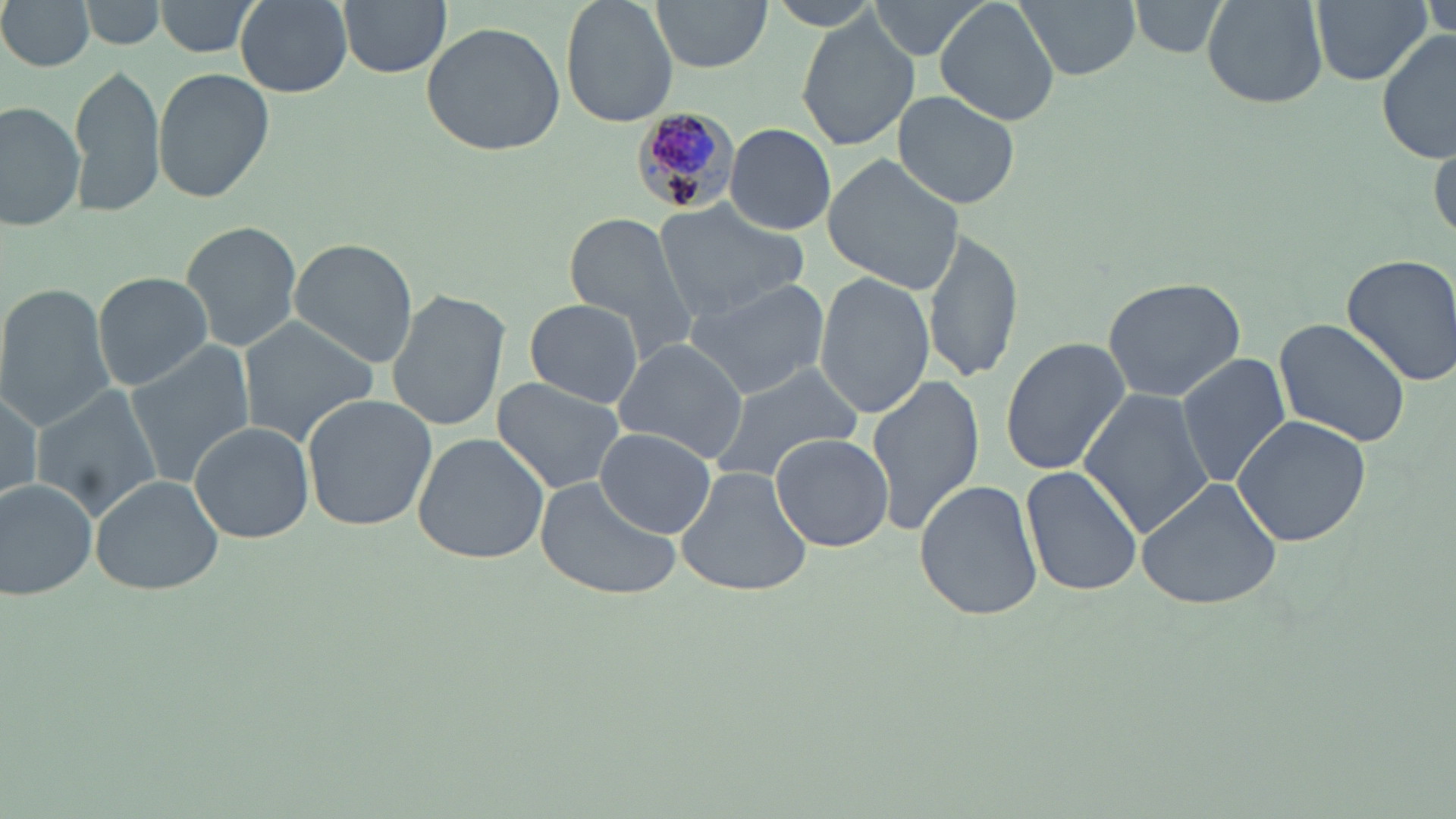

Summary:
  - Coordinate format: approximate bounding boxes as [x1, y1, x2, y2] in pixels
  - Plasmodium malariae-infected red blood cell locations: [630, 106, 742, 220]
  - Uninfected red blood cell locations: [0, 0, 98, 72], [82, 0, 167, 49], [154, 0, 263, 56], [338, 0, 450, 78], [560, 0, 679, 127], [650, 0, 773, 72], [867, 0, 992, 64], [936, 0, 1059, 126], [1015, 0, 1140, 81], [1122, 0, 1239, 58], [1206, 0, 1330, 106], [1310, 0, 1429, 85], [1423, 0, 1454, 42], [235, 1, 353, 97], [797, 14, 918, 153], [421, 21, 565, 158], [1376, 31, 1454, 165], [70, 64, 168, 221], [152, 66, 274, 203], [892, 90, 1022, 210], [1, 101, 85, 232], [725, 123, 836, 236], [1429, 131, 1455, 245], [822, 154, 965, 295], [654, 199, 810, 320], [562, 211, 702, 370], [180, 219, 303, 355], [922, 228, 1023, 387], [287, 238, 419, 367], [1340, 251, 1456, 389], [815, 271, 934, 420], [92, 272, 214, 391], [1101, 275, 1247, 402], [683, 278, 829, 399], [0, 284, 115, 434], [386, 289, 510, 433], [524, 298, 644, 408], [237, 317, 380, 446], [1274, 318, 1413, 448], [612, 337, 752, 465], [998, 338, 1130, 476], [124, 341, 255, 486], [1175, 353, 1290, 490], [705, 362, 864, 483], [867, 374, 986, 536], [491, 378, 626, 496], [30, 385, 162, 523], [1, 386, 46, 507], [1080, 387, 1212, 543], [302, 393, 438, 532], [1231, 413, 1374, 548], [188, 421, 314, 543], [596, 430, 716, 539], [411, 432, 552, 565], [770, 433, 894, 552], [1023, 462, 1143, 599], [674, 465, 813, 598], [89, 474, 227, 595], [0, 476, 101, 600], [1136, 476, 1284, 610], [534, 477, 683, 599], [914, 479, 1044, 621]
  - Slide-level diagnosis: Plasmodium malariae
  - Field of view: single
  - Modality: light microscopy
  - Magnification: 1000x
  - Preparation: thin blood smear
  - Image size: 1456×819 pixels
  - Stain: May-Grünwald-Giemsa